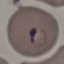
Summary:
  - Malaria status: parasitized
  - Image type: cell patch, automatically extracted from a larger field of view and resized to 64 × 64 pixels
  - Stain: Giemsa
  - Preparation: thin blood film
  - Capture: smartphone camera at the microscope eyepiece